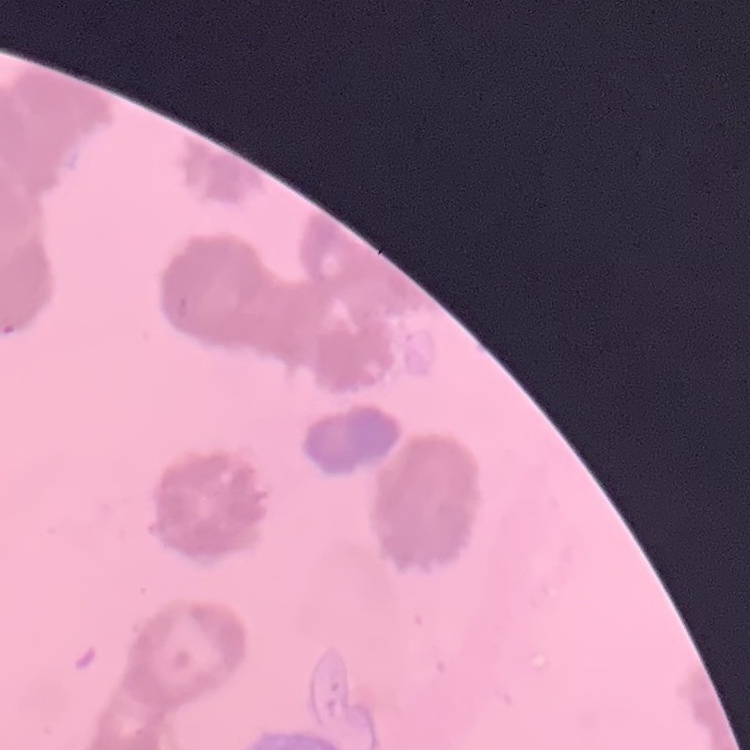 The red blood cells show rouleaux formation. One tile cut from a larger photomicrograph. Stained with either Field's or Giemsa. Thin peripheral smear.